Report the malaria status of this cell.
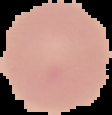
It is uninfected.

preparation: thin blood film
image_type: segmented cell region on a black background
image_size: 112×115 pixels